Assess this cell for malaria.
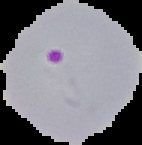

It is parasitized.

The area outside the segmented cell region is set to black. Image is 142×145 pixels. From a thin blood film.